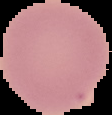

Malaria status: uninfected. From a thin blood film. Segmented cell region on a black background. Image is 112×115 pixels.